Point out each malaria parasite.
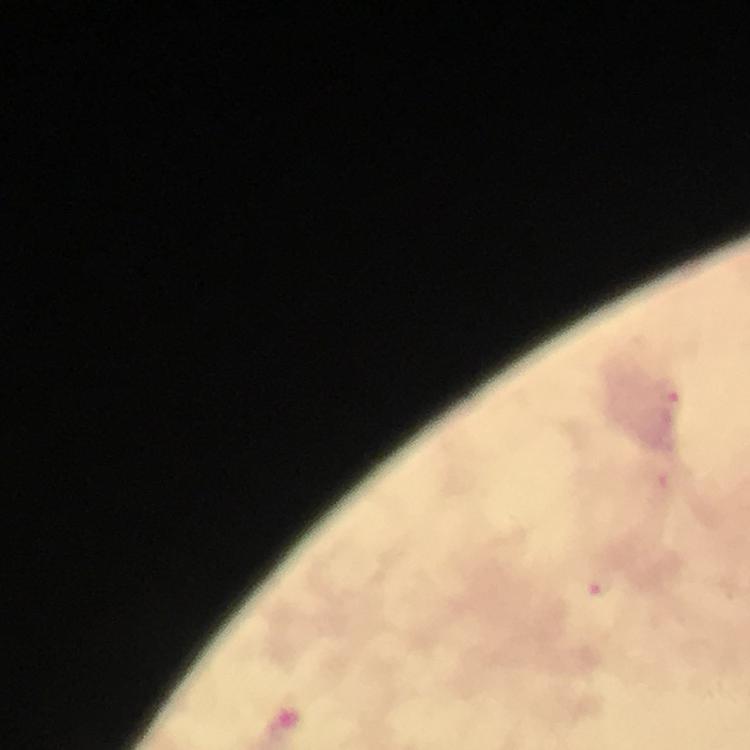

Approximate centers as (x, y) in pixels.
Malaria parasites: (670, 390), (602, 584).

Thick blood film. Smartphone photograph taken through a microscope. From a malaria diagnostic workup. Immersion oil applied. Giemsa-stained preparation. Image is 750×750 pixels. At 100x magnification. A crop from one field of view.